State which cell type is depicted.
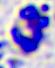
This is a leukocyte.

{
  "magnification": "400x",
  "modality": "micrograph"
}